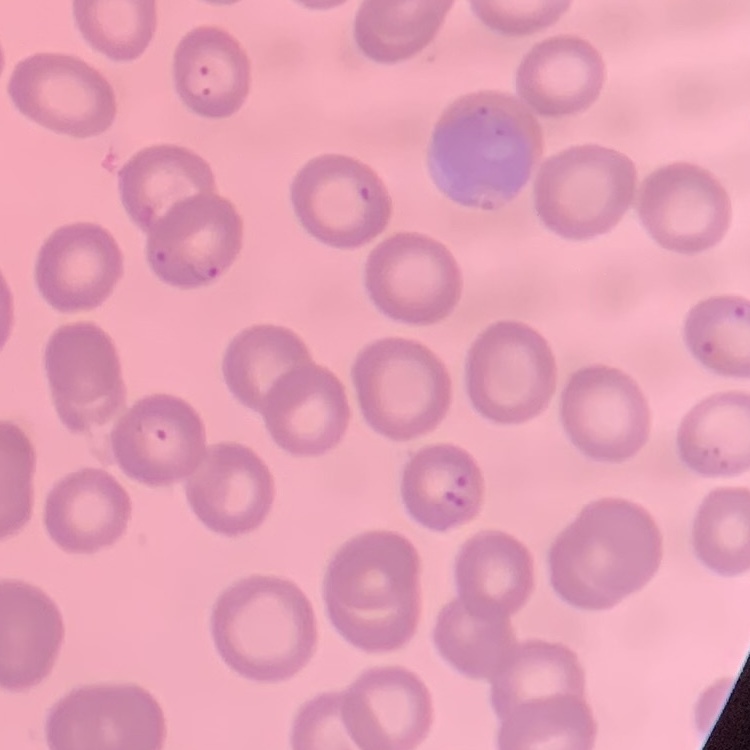

erythrocyte morphology = no rouleaux formation
stain = Field's or Giemsa
image type = one tile cut from a larger photomicrograph
preparation = thin blood smear